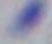
magnification = 1000x
identification = Toxoplasma gondii
modality = micrograph